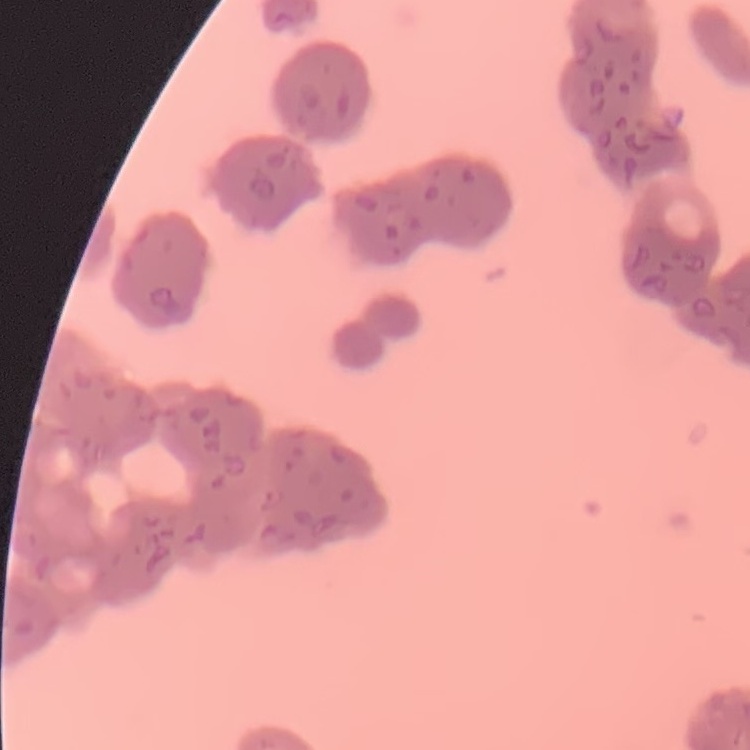

The red blood cells show rouleaux formation. Stained with either Field's or Giemsa. Square crop of a larger photomicrograph. Thin blood film.